Report the malaria status of this cell.
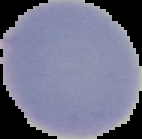
Uninfected.

Summary:
  - Image type: segmented cell region on a black background
  - Preparation: thin blood smear
  - Image size: 142×139 pixels